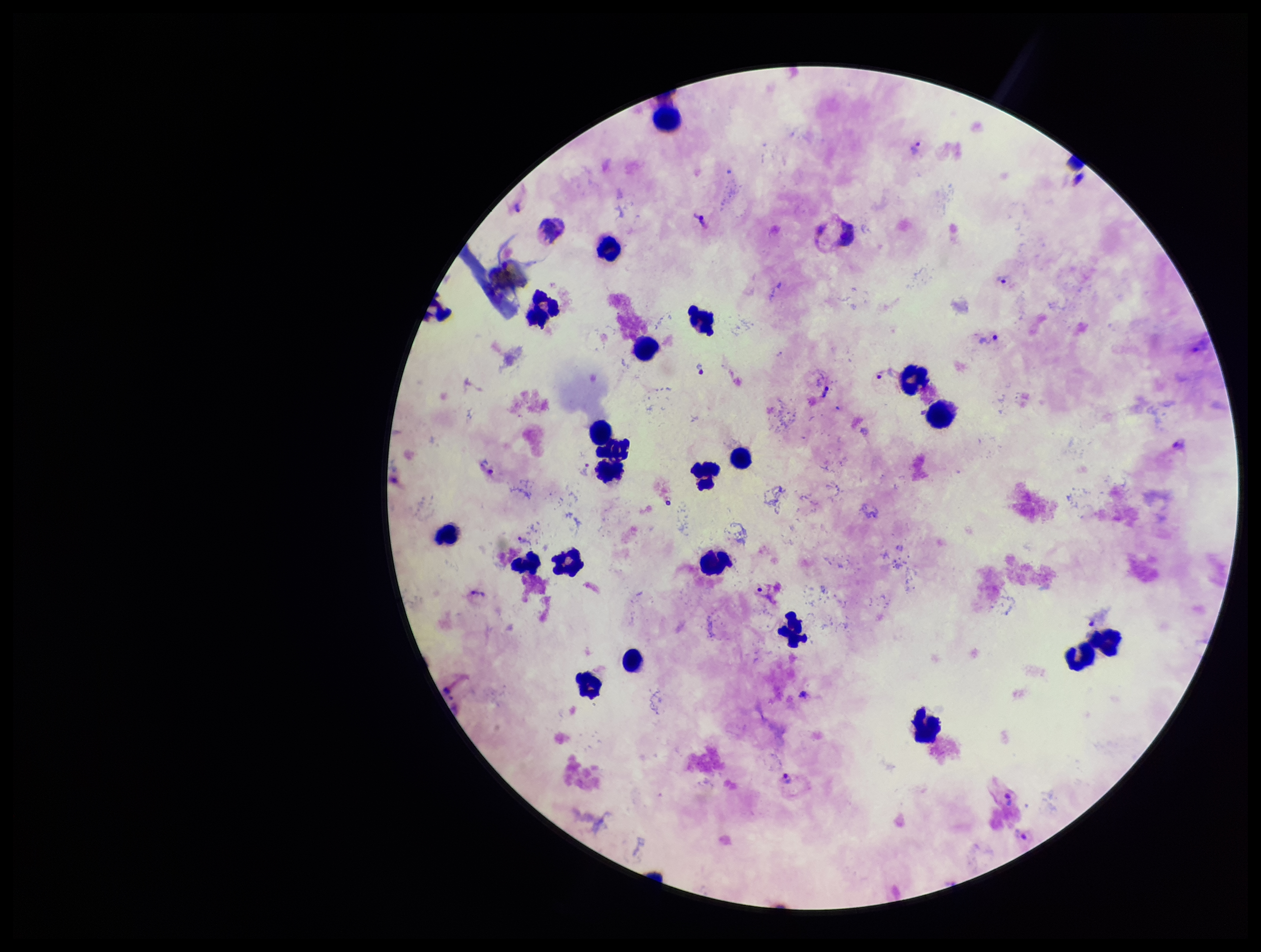
Summary:
  - Preparation: thick
  - Plasmodium parasites: identified
  - Field of view: one from this slide
  - Patient malaria status: positive
  - Parasite count: 12
  - Species reported for this patient: Plasmodium vivax
  - Leukocyte count: 24
  - Image size: 1261×952 pixels
  - Capture: smartphone photograph through the microscope eyepiece
  - Stain: Giemsa